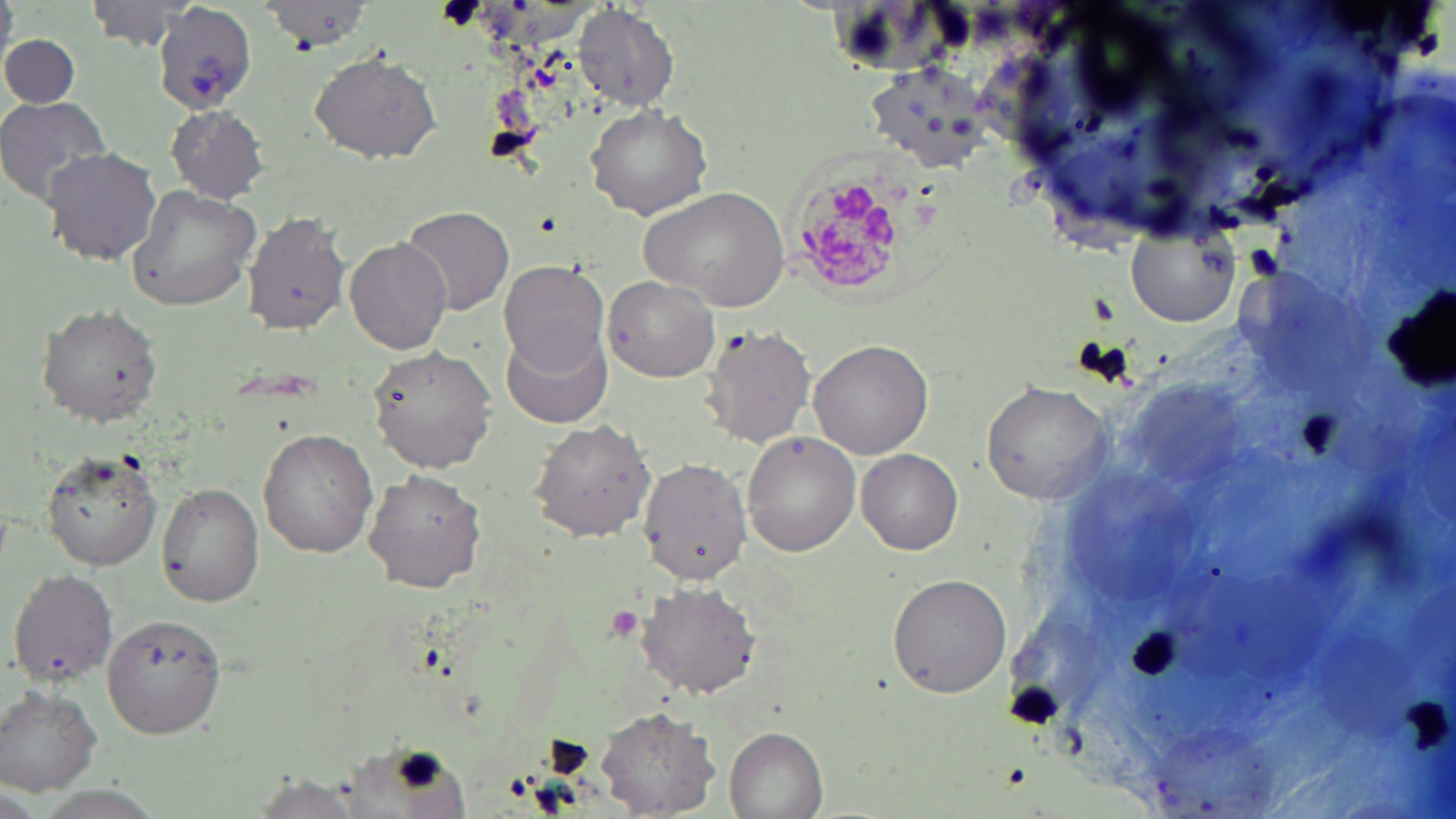

Summary:
  - Coordinate format: approximate bounding boxes as [x1, y1, x2, y2] in pixels
  - Plasmodium malariae-infected red blood cell locations: [791, 170, 922, 292]
  - Platelet locations: [1242, 240, 1285, 284], [603, 606, 644, 640]
  - Uninfected red blood cell locations: [82, 0, 194, 49], [263, 2, 373, 51], [153, 4, 258, 113], [573, 6, 678, 111], [0, 30, 81, 112], [309, 52, 441, 163], [0, 96, 112, 206], [585, 102, 713, 220], [166, 107, 270, 200], [41, 145, 162, 266], [126, 184, 262, 313], [640, 185, 790, 312], [402, 206, 514, 317], [241, 209, 352, 334], [1129, 227, 1240, 329], [344, 237, 451, 353], [499, 260, 611, 378], [603, 275, 720, 383], [1386, 286, 1455, 393], [37, 303, 162, 426], [702, 324, 816, 447], [503, 333, 613, 427], [807, 337, 932, 460], [367, 344, 497, 472], [981, 379, 1114, 504], [528, 418, 657, 540], [259, 428, 379, 558], [741, 431, 861, 556], [40, 448, 164, 572], [858, 449, 962, 555], [638, 456, 754, 586], [365, 468, 487, 593], [156, 482, 265, 607], [8, 567, 118, 684], [886, 572, 1014, 698], [636, 580, 762, 698], [105, 614, 226, 735], [1, 685, 104, 795], [596, 705, 721, 816], [724, 725, 829, 819], [248, 773, 367, 819]
  - Slide-level diagnosis: Plasmodium malariae
  - Magnification: 1000x
  - Modality: light microscopy
  - Field of view: one of a larger specimen
  - Stain: May-Grünwald-Giemsa
  - Image size: 1456×819 pixels
  - Preparation: thin blood film